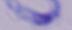
{
  "identification": "trypanosome",
  "magnification": "1000x",
  "modality": "photomicrograph"
}